Find each parasitized RBC.
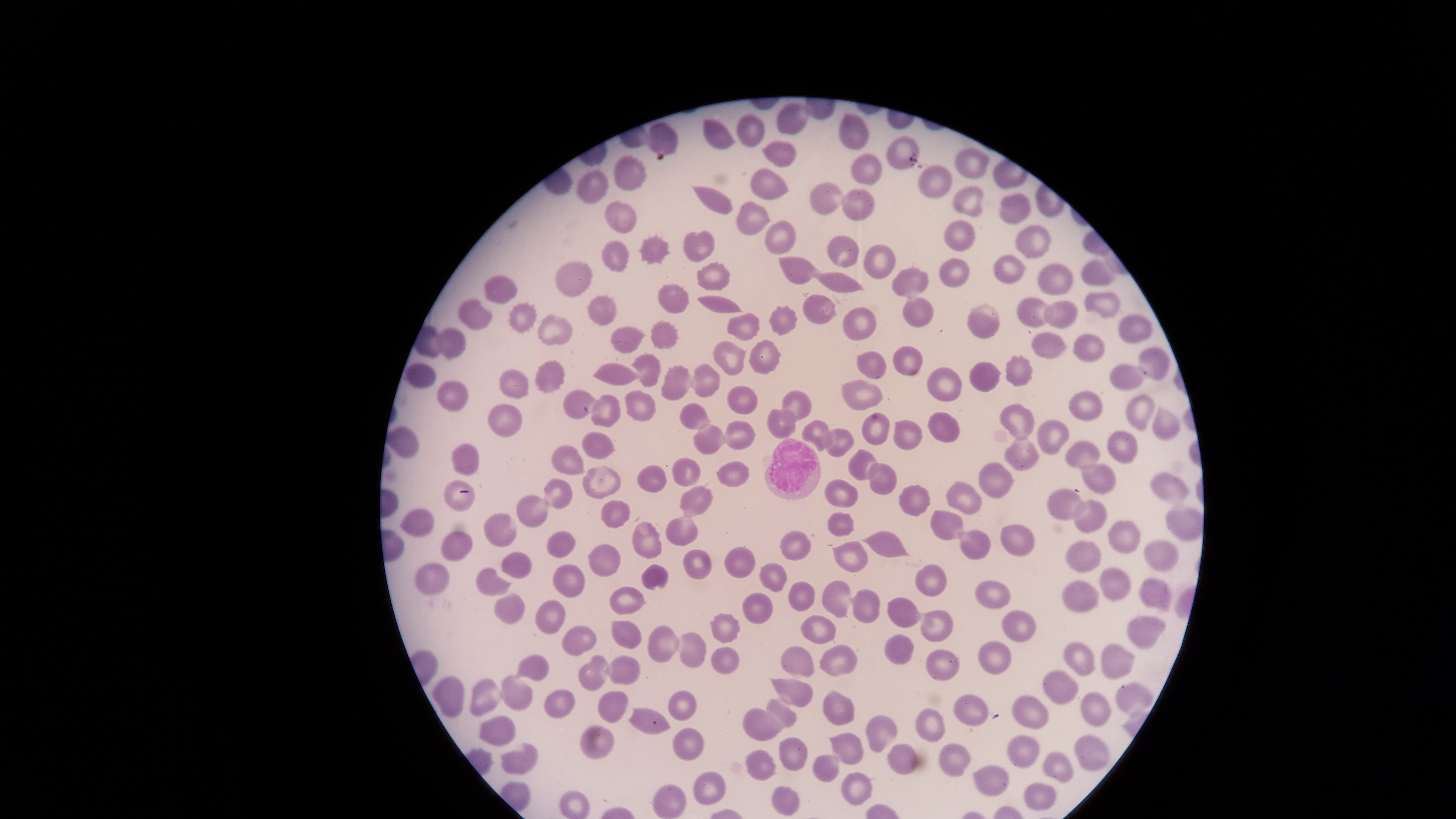
No parasitized RBCs identified.

visible_region: circular
preparation: thin smear of blood
field_of_view: single
uninfected_RBCs: 'approximate bounding boxes as (left, top, right, bottom) in pixels: (776, 101, 811, 134), (736, 113, 765, 147), (838, 113, 869, 149), (703, 118, 735, 149), (648, 122, 678, 156), (761, 140, 796, 168), (954, 147, 989, 179), (851, 154, 882, 185), (613, 156, 646, 191), (918, 163, 952, 198), (749, 168, 788, 199), (575, 170, 609, 203), (810, 182, 847, 215), (952, 186, 983, 217), (692, 187, 732, 215), (841, 189, 874, 221), (998, 193, 1031, 225), (736, 200, 770, 235), (605, 201, 636, 233), (765, 220, 795, 255), (943, 220, 975, 251), (1015, 224, 1051, 260), (682, 230, 714, 261), (637, 233, 671, 265), (827, 235, 860, 268), (601, 241, 628, 272), (863, 245, 895, 278), (992, 254, 1025, 284), (778, 257, 820, 285), (940, 258, 968, 287), (1081, 259, 1114, 285), (554, 260, 593, 297), (696, 262, 731, 290), (1037, 262, 1072, 296), (891, 268, 929, 298), (807, 271, 861, 292), (484, 275, 517, 303), (658, 285, 689, 312), (1084, 292, 1121, 318), (696, 294, 740, 313), (587, 296, 616, 325), (802, 296, 835, 324), (902, 297, 933, 327), (1017, 298, 1052, 326), (458, 299, 492, 330), (1044, 301, 1078, 328), (967, 304, 999, 338), (508, 305, 536, 332), (768, 305, 799, 336), (843, 306, 876, 340), (726, 313, 759, 340), (537, 315, 572, 346), (1118, 315, 1152, 343), (649, 321, 678, 348), (610, 326, 646, 353), (436, 328, 465, 359), (1031, 331, 1066, 359), (1072, 333, 1105, 362), (748, 339, 782, 376), (714, 341, 745, 376), (893, 346, 923, 376), (1138, 346, 1169, 383), (856, 351, 886, 379), (634, 353, 660, 387), (1004, 355, 1034, 386), (534, 360, 565, 394), (969, 361, 1000, 392), (404, 362, 436, 388), (593, 363, 643, 385), (690, 364, 719, 397), (1110, 364, 1146, 392), (660, 365, 692, 401), (926, 367, 961, 402), (498, 368, 528, 399), (842, 379, 884, 410), (436, 380, 469, 411), (726, 386, 759, 414), (562, 390, 603, 420), (623, 390, 655, 422), (781, 391, 813, 423), (1069, 391, 1103, 421), (590, 394, 620, 427), (1124, 395, 1154, 432), (488, 403, 522, 436), (679, 403, 710, 430), (999, 404, 1035, 442), (1152, 405, 1180, 442), (766, 409, 796, 439), (861, 412, 889, 446), (926, 412, 961, 443), (802, 419, 832, 451), (893, 419, 924, 451), (1036, 419, 1069, 456), (722, 421, 754, 450), (693, 425, 726, 456), (385, 427, 418, 458), (822, 428, 853, 457), (1107, 430, 1139, 464), (582, 432, 615, 460), (1005, 437, 1037, 470), (1066, 442, 1099, 470), (451, 444, 479, 475), (551, 444, 583, 474), (848, 447, 879, 480), (671, 458, 700, 486), (717, 463, 752, 487), (867, 463, 897, 495), (978, 463, 1013, 498), (1078, 463, 1116, 494), (636, 465, 667, 493), (582, 467, 622, 500), (1151, 472, 1189, 505), (543, 479, 572, 509), (824, 479, 858, 508), (945, 481, 980, 515), (898, 485, 930, 517), (679, 486, 712, 517), (1047, 489, 1087, 520), (517, 495, 549, 528), (601, 498, 630, 528), (1072, 499, 1107, 534), (1166, 506, 1204, 541), (400, 507, 435, 537), (929, 510, 963, 539), (827, 511, 854, 536), (663, 512, 698, 546), (483, 514, 515, 547), (1107, 520, 1140, 553), (632, 522, 661, 558), (1000, 524, 1034, 556), (780, 529, 812, 560), (862, 530, 907, 557), (959, 530, 991, 560), (441, 531, 473, 561), (545, 531, 575, 558), (1065, 539, 1101, 572), (1142, 539, 1180, 572), (830, 541, 867, 572), (589, 545, 619, 576), (724, 546, 755, 577), (684, 548, 711, 579), (500, 552, 531, 579), (553, 562, 584, 597), (759, 562, 787, 592), (415, 563, 448, 594), (640, 564, 668, 591), (914, 565, 947, 597), (1100, 567, 1130, 600), (475, 568, 511, 596), (1139, 577, 1171, 612), (1062, 580, 1100, 612), (789, 581, 815, 611), (822, 581, 851, 617), (975, 581, 1011, 608), (609, 585, 645, 614), (848, 589, 879, 624), (741, 593, 773, 624), (494, 594, 525, 624), (886, 595, 921, 628), (534, 600, 565, 634), (1001, 609, 1036, 642), (919, 610, 952, 641), (709, 612, 740, 644), (801, 614, 835, 645), (1126, 616, 1166, 649), (610, 620, 642, 648), (562, 625, 597, 656), (647, 626, 680, 662), (677, 632, 707, 668), (884, 635, 914, 664), (978, 641, 1011, 675), (1062, 641, 1095, 675), (1101, 643, 1137, 680), (780, 645, 814, 676), (818, 645, 857, 676), (710, 647, 740, 675), (926, 650, 958, 681), (515, 653, 550, 680), (577, 654, 609, 691), (602, 655, 640, 684), (1042, 669, 1078, 704), (431, 676, 465, 717), (499, 676, 533, 709), (771, 678, 813, 707), (468, 679, 503, 715), (1117, 681, 1152, 715), (544, 688, 575, 719), (821, 689, 854, 725), (597, 690, 629, 723), (668, 691, 696, 720), (1081, 692, 1110, 727), (953, 694, 988, 725), (1010, 695, 1049, 729), (766, 698, 797, 727), (627, 708, 671, 734), (743, 708, 783, 741), (915, 708, 945, 741), (479, 714, 515, 747), (865, 715, 897, 751), (579, 724, 614, 759), (672, 728, 703, 760), (828, 733, 863, 764), (1007, 735, 1040, 766), (1074, 735, 1110, 772), (778, 736, 807, 771), (501, 742, 539, 774), (887, 743, 917, 774), (938, 743, 972, 777), (745, 750, 775, 780), (1041, 752, 1075, 783), (812, 756, 838, 782), (971, 764, 1009, 796), (840, 771, 872, 807), (692, 772, 725, 804), (1023, 782, 1056, 811), (654, 784, 685, 818), (771, 787, 799, 816), (558, 790, 590, 818)'
capture: smartphone photograph through the microscope eyepiece
WBCs: 'approximate bounding boxes as (left, top, right, bottom) in pixels: (764, 437, 822, 500)'
image_size: 1456×819 pixels
stain: Giemsa